Describe the morphology of the red blood cells.
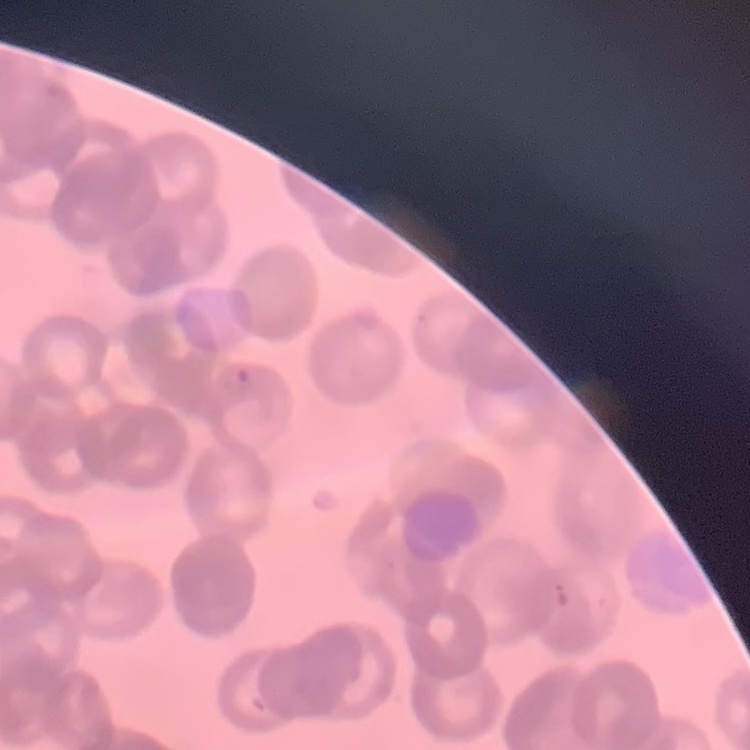

Rouleaux formation.

{
  "image_type": "square crop of a larger photomicrograph",
  "stain": "Field's or Giemsa",
  "preparation": "thin blood film"
}